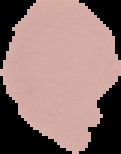

preparation = thin blood film
image type = segmented cell region with the area outside set to black
result = no malaria parasites detected
image size = 121×154 pixels